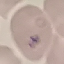

Summary:
  - Malaria status: uninfected
  - Preparation: thin smear
  - Image type: automatically extracted cell patch, resized to 64 × 64 pixels
  - Capture: smartphone camera at the microscope eyepiece
  - Stain: Giemsa